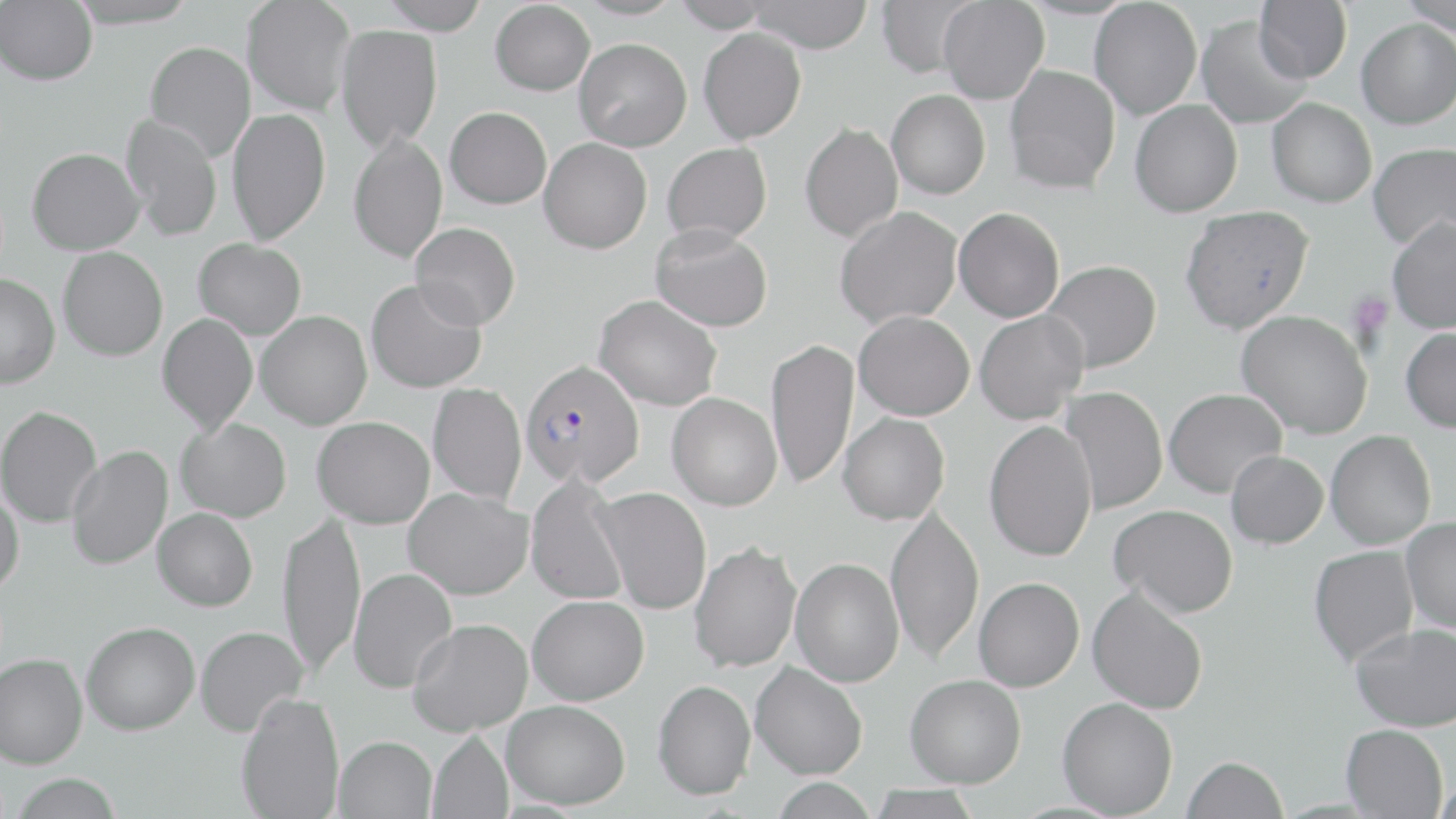

Approximate bounding boxes as (x1,y1)-(x2,y2) corner pairs in pixels. Plasmodium falciparum-infected red blood cell locations: (520,358)-(645,487). Uninfected red blood cell locations: (66,0)-(200,29), (241,0)-(356,114), (378,0)-(491,34), (670,0)-(774,32), (745,0)-(874,53), (875,0)-(980,78), (1089,0)-(1202,120), (1255,0)-(1353,83), (1398,0)-(1456,36), (0,1)-(98,85), (490,1)-(596,96), (938,1)-(1049,104), (1196,15)-(1311,129), (1356,19)-(1456,129), (335,24)-(443,150), (698,27)-(807,144), (574,38)-(692,151), (145,41)-(256,161), (1004,64)-(1121,192), (887,89)-(990,200), (1267,97)-(1377,207), (1130,99)-(1242,217), (445,106)-(552,208), (227,107)-(331,245), (120,114)-(223,242), (799,122)-(903,242), (348,131)-(447,264), (539,137)-(652,253), (662,142)-(772,244), (1368,142)-(1456,251), (27,147)-(145,254), (1180,205)-(1314,333), (835,206)-(963,329), (954,207)-(1065,322), (1387,215)-(1456,333), (410,221)-(521,329), (650,223)-(773,332), (193,238)-(307,340), (57,246)-(168,361), (1041,260)-(1161,373), (0,274)-(60,388), (366,278)-(487,393), (593,294)-(722,411), (256,310)-(372,429), (853,310)-(974,420), (974,310)-(1089,424), (1237,310)-(1373,439), (157,313)-(258,435), (1401,326)-(1456,433), (766,338)-(859,489), (427,383)-(527,504), (1060,386)-(1167,515), (1164,388)-(1287,497), (667,392)-(782,510), (0,405)-(102,527), (838,412)-(950,525), (313,416)-(435,528), (175,417)-(292,522), (984,419)-(1098,561), (1326,430)-(1436,549), (67,445)-(173,571), (1226,450)-(1328,548), (525,473)-(630,606), (0,483)-(24,595), (593,486)-(712,614), (404,487)-(533,599), (885,504)-(984,664), (1110,504)-(1238,617), (153,508)-(258,611), (277,512)-(366,676), (1401,516)-(1456,634), (689,541)-(801,673), (1309,545)-(1418,665), (790,557)-(904,686), (349,568)-(457,693), (974,576)-(1085,692), (1087,585)-(1208,714), (527,595)-(649,705), (408,618)-(533,736), (81,621)-(200,735), (1351,623)-(1456,731), (195,625)-(308,736), (0,652)-(88,768), (750,661)-(868,779), (905,674)-(1026,787), (653,679)-(756,800), (236,692)-(344,819), (1057,697)-(1178,818), (502,699)-(630,809), (1341,723)-(1448,818), (427,731)-(513,819), (334,736)-(436,819), (1182,756)-(1288,818), (10,774)-(123,819), (770,777)-(878,819), (865,785)-(984,819). Platelet locations: (1347,291)-(1393,340). Slide-level diagnosis: Plasmodium falciparum. Captured at 1000x magnification. May-Grünwald-Giemsa stain. Light microscopy. Single field of view. Thin blood smear. Image is 1456×819 pixels.